Report the malaria status of this cell.
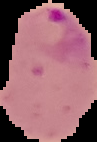
Parasitized.

Summary:
  - Image size: 97×142 pixels
  - Preparation: thin blood film
  - Image type: cell region segmented out of the field of view; surrounding area masked to black